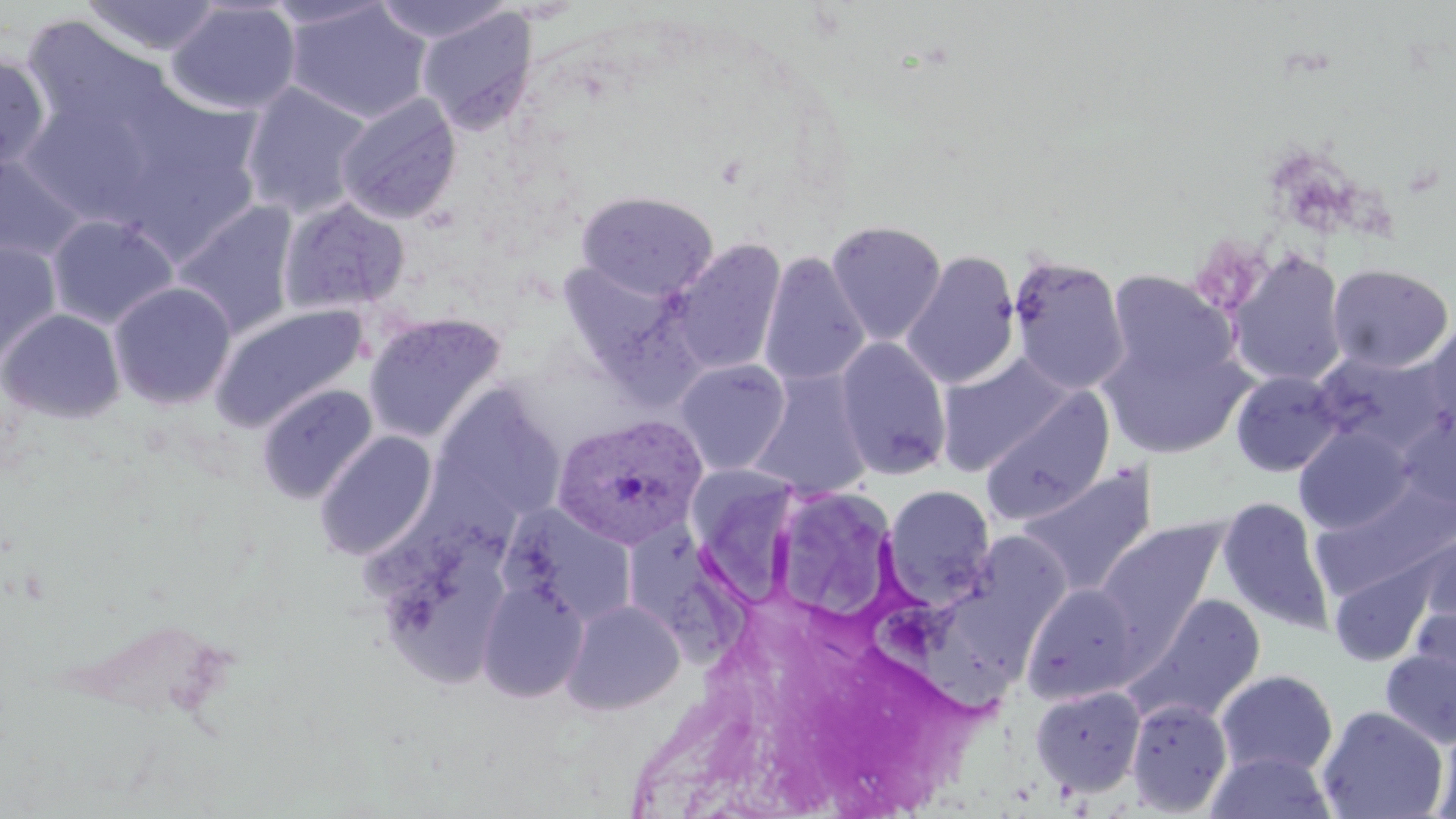
Summary:
  - Coordinate format: approximate bounding boxes as (x1, y1, x2, y2) in pixels
  - Plasmodium vivax-infected red blood cell locations: (554, 414, 708, 549)
  - Uninfected red blood cell locations: (80, 0, 225, 56), (261, 0, 394, 30), (370, 0, 515, 45), (166, 1, 301, 116), (284, 2, 432, 124), (43, 5, 217, 100), (417, 8, 538, 134), (20, 17, 177, 146), (0, 54, 51, 173), (241, 83, 374, 220), (336, 93, 462, 225), (25, 98, 151, 220), (0, 152, 89, 266), (141, 156, 263, 253), (577, 190, 718, 301), (279, 198, 410, 317), (172, 202, 299, 340), (47, 215, 178, 329), (825, 220, 946, 345), (667, 238, 787, 377), (0, 240, 62, 368), (1227, 248, 1349, 387), (901, 251, 1021, 390), (759, 253, 870, 388), (1008, 255, 1130, 396), (557, 260, 688, 378), (1326, 263, 1454, 373), (1107, 270, 1236, 385), (108, 282, 236, 410), (212, 304, 368, 432), (0, 308, 125, 424), (363, 312, 507, 445), (1424, 318, 1456, 437), (1099, 332, 1250, 459), (834, 337, 952, 479), (1310, 349, 1452, 458), (936, 355, 1072, 475), (674, 359, 791, 475), (1230, 370, 1344, 478), (749, 371, 873, 499), (432, 383, 566, 523), (257, 384, 377, 504), (980, 388, 1115, 526), (1294, 426, 1414, 535), (314, 431, 437, 561), (690, 459, 803, 611), (1016, 466, 1157, 596), (1311, 480, 1456, 601), (883, 484, 996, 607), (783, 487, 897, 623), (1216, 497, 1333, 634), (504, 506, 639, 625), (1096, 519, 1230, 649), (621, 523, 755, 679), (1416, 525, 1456, 640), (966, 532, 1072, 653), (1328, 555, 1439, 666), (476, 579, 589, 702), (1021, 583, 1144, 704), (1128, 594, 1266, 724), (561, 598, 685, 715), (862, 600, 1014, 725), (1379, 646, 1456, 750), (1216, 669, 1339, 778), (1030, 685, 1146, 798), (1126, 698, 1233, 816), (1317, 705, 1449, 819), (1431, 721, 1456, 819), (1205, 750, 1337, 818)
  - Slide-level diagnosis: Plasmodium vivax
  - Image size: 1456×819 pixels
  - Magnification: 1000x
  - Modality: light microscopy
  - Preparation: thin blood smear
  - Stain: May-Grünwald-Giemsa
  - Field of view: single